Describe the morphology of the erythrocytes.
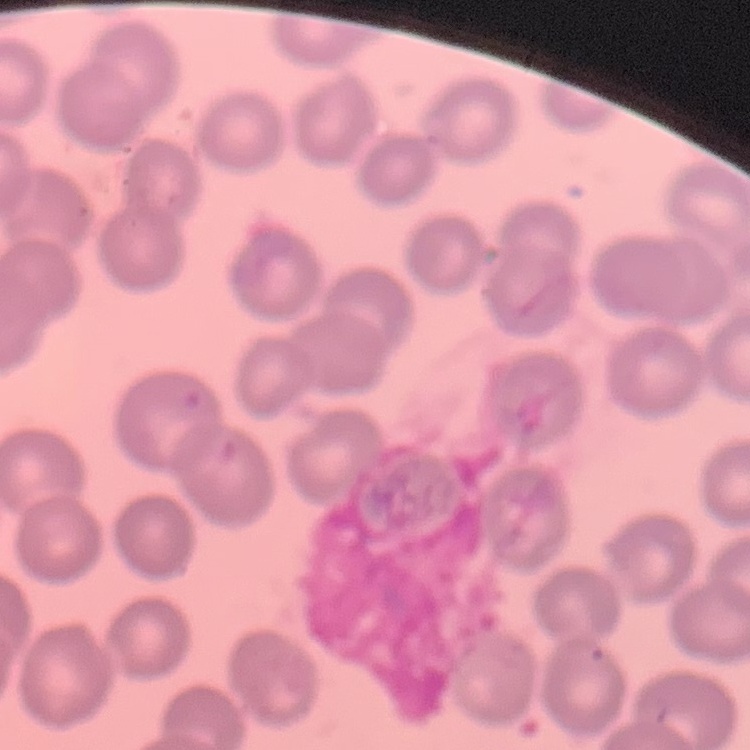
No rouleaux formation.

stain = Field's or Giemsa
image type = one tile cut from a larger photomicrograph
preparation = thin blood smear